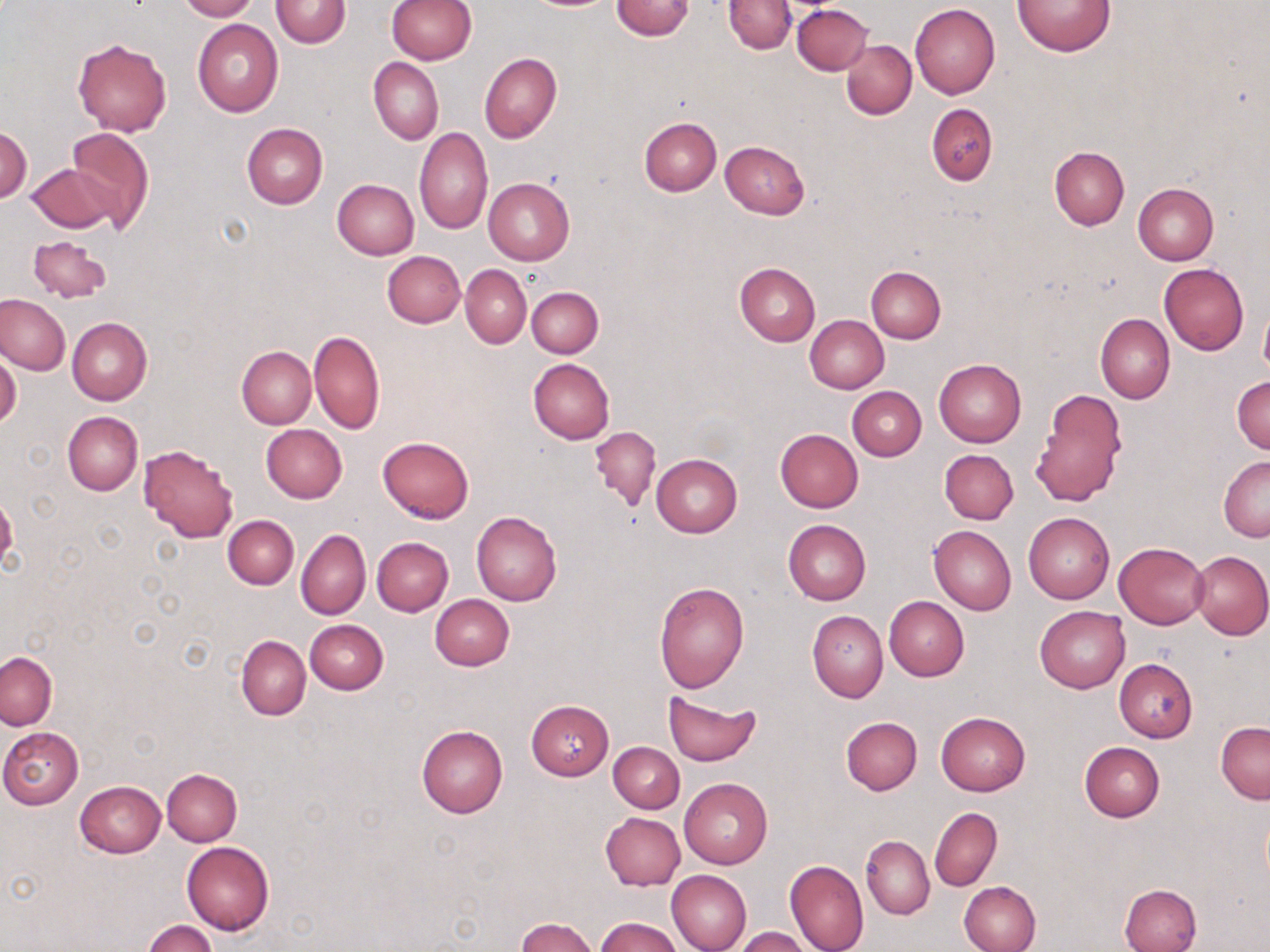
Summary:
  - Coordinate format: approximate bounding boxes as [x1, y1, x2, y2] in pixels
  - Uninfected red blood cell locations: [177, 0, 258, 21], [271, 0, 351, 48], [386, 0, 476, 64], [610, 0, 695, 40], [1013, 0, 1116, 56], [723, 1, 795, 54], [791, 3, 872, 74], [910, 3, 1000, 99], [192, 19, 284, 117], [72, 38, 172, 136], [842, 40, 917, 119], [479, 53, 561, 143], [368, 57, 443, 145], [927, 104, 999, 184], [638, 116, 721, 195], [241, 123, 328, 209], [1, 125, 31, 203], [64, 126, 154, 234], [414, 126, 493, 233], [721, 141, 810, 218], [1049, 146, 1129, 229], [26, 162, 116, 233], [484, 176, 575, 264], [332, 179, 419, 259], [1134, 183, 1218, 266], [28, 235, 112, 304], [382, 250, 465, 328], [734, 262, 821, 345], [1159, 264, 1248, 355], [461, 265, 531, 348], [866, 267, 946, 343], [527, 286, 604, 358], [0, 293, 70, 375], [1259, 302, 1270, 378], [1095, 313, 1175, 404], [804, 315, 888, 394], [67, 318, 151, 405], [309, 330, 385, 434], [236, 345, 316, 429], [0, 353, 21, 431], [528, 358, 614, 444], [933, 359, 1025, 446], [1231, 376, 1269, 454], [847, 386, 926, 461], [1028, 389, 1128, 509], [62, 411, 143, 495], [261, 425, 347, 503], [590, 426, 660, 512], [775, 429, 864, 512], [378, 436, 474, 523], [138, 444, 238, 542], [940, 449, 1019, 524], [651, 454, 742, 537], [1219, 456, 1270, 542], [471, 511, 562, 606], [1023, 512, 1114, 604], [223, 514, 299, 589], [783, 520, 871, 605], [929, 526, 1016, 615], [297, 528, 370, 620], [371, 537, 453, 616], [1114, 542, 1209, 628], [1190, 550, 1269, 640], [654, 580, 749, 692], [431, 594, 514, 670], [884, 596, 968, 682], [1035, 606, 1130, 692], [808, 610, 888, 702], [305, 620, 388, 694], [236, 636, 311, 719], [0, 653, 57, 730], [1114, 659, 1198, 742], [663, 692, 762, 766], [525, 700, 615, 781], [935, 712, 1030, 796], [841, 717, 922, 795], [1216, 721, 1269, 803], [417, 725, 508, 818], [0, 727, 84, 808], [609, 741, 684, 813], [1079, 741, 1165, 822], [162, 768, 242, 845], [679, 778, 773, 869], [75, 781, 167, 858], [929, 807, 1002, 892], [599, 812, 685, 890], [862, 836, 934, 919], [181, 841, 273, 935], [785, 860, 868, 952], [667, 870, 752, 952], [960, 881, 1041, 952], [1120, 883, 1201, 952], [515, 917, 599, 952], [596, 917, 682, 952], [143, 919, 216, 952], [733, 927, 810, 952]
  - Slide-level diagnosis: negative for blood parasites
  - Stain: May-Grünwald-Giemsa
  - Field of view: single
  - Image size: 1270×952 pixels
  - Magnification: 1000x
  - Preparation: thin blood smear
  - Modality: optical microscopy